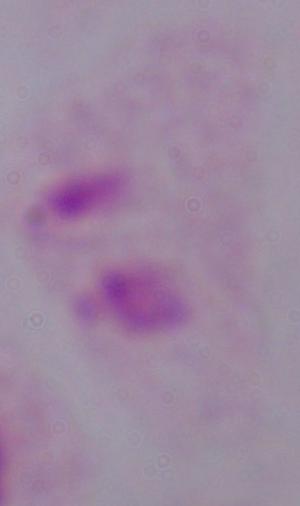 Micrograph. Captured at 1000x magnification. A trichomonad is seen.